Classify this cell by malaria status.
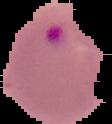

Parasitized.

preparation: thin blood film
image_size: 112×124 pixels
image_type: cell region segmented out of the field of view; surrounding area masked to black